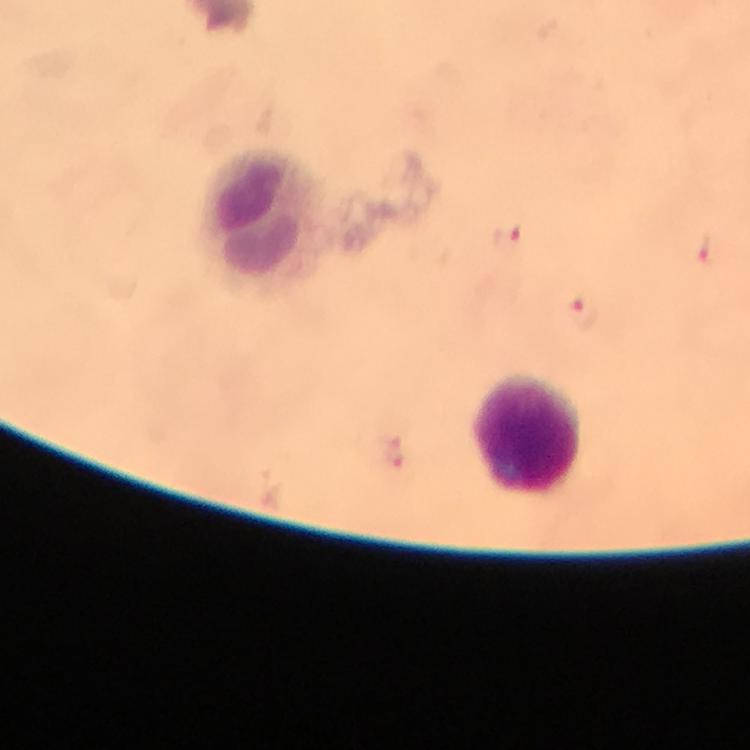
Approximate centers as (x, y) in pixels. Leukocyte locations: (261, 221), (526, 432). Plasmodium parasite locations: (507, 238), (705, 250), (581, 313). Giemsa-stained preparation. Photographed through the microscope with a smartphone camera. Thick smear. Image is 750×750 pixels. Immersion oil applied. At 100x magnification. From a malaria diagnostic workup. A crop from one field of view.